Report the malaria status of this cell.
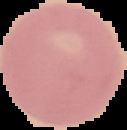
It is uninfected.

Summary:
  - Image size: 127×130 pixels
  - Image type: segmented cell region with the area outside set to black
  - Preparation: thin blood film